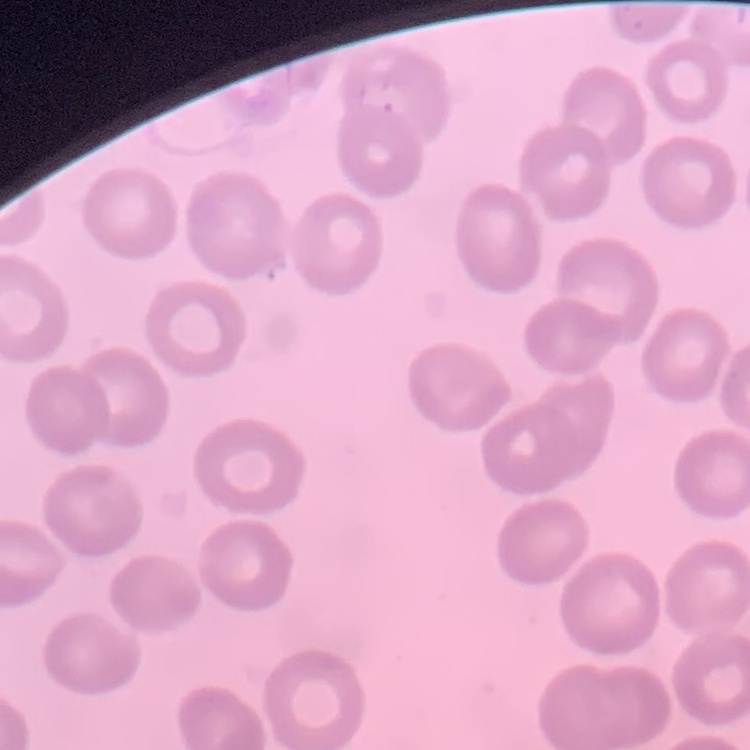
erythrocyte morphology = no rouleaux formation
preparation = thin blood film
image type = square crop of a larger photomicrograph
stain = Field's or Giemsa